Comment on the morphology of the red blood cells.
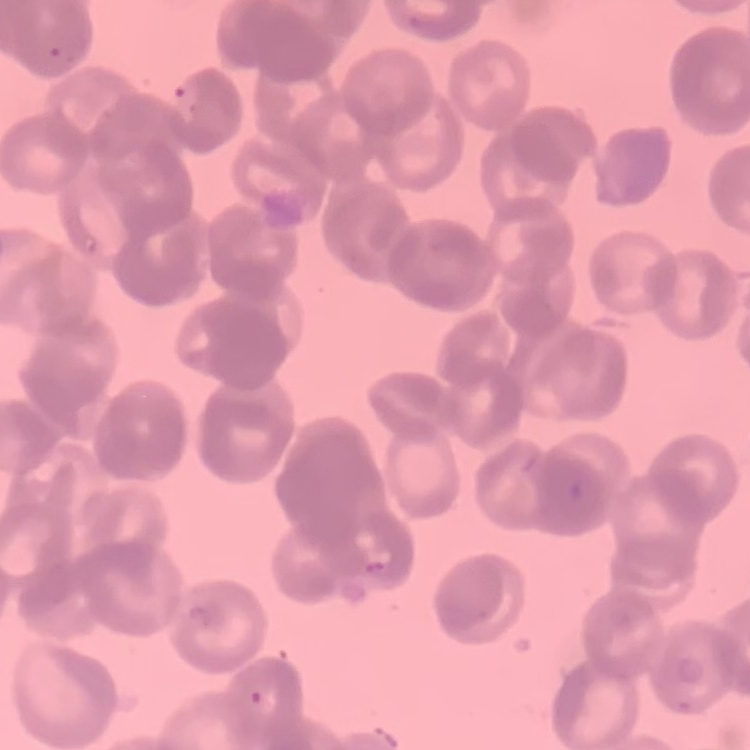

Rouleaux formation.

preparation = thin peripheral smear
stain = Field's or Giemsa
image type = square crop of a larger photomicrograph